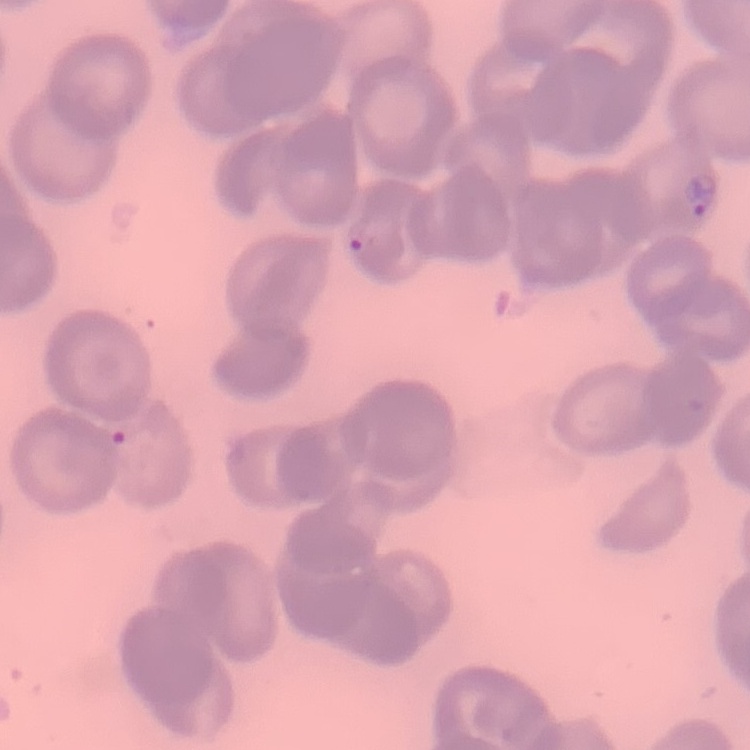

{
  "red_blood_cell_morphology": "no rouleaux formation",
  "stain": "Field's or Giemsa",
  "preparation": "thin blood film",
  "image_type": "square crop of a larger photomicrograph"
}